Locate and identify every blood parasite.
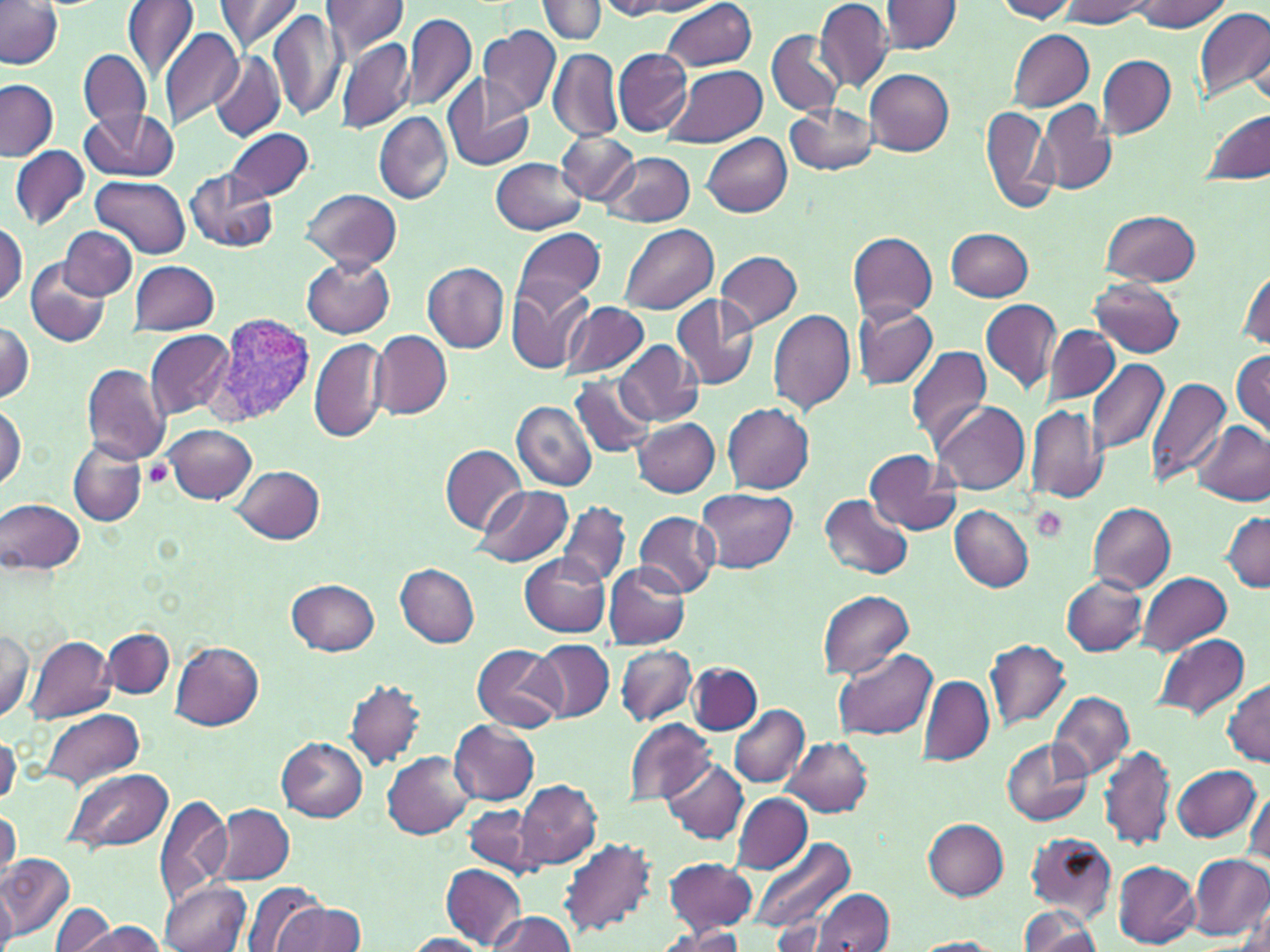
Approximate bounding boxes as (x1, y1, x2, y2) in pixels.
Plasmodium vivax-infected red blood cells: (207, 312, 317, 428).
No Plasmodium falciparum, Plasmodium ovale, Plasmodium malariae, Babesia divergens, or Trypanosoma brucei observed.

Uninfected red blood cell locations: (123, 0, 199, 80), (319, 0, 410, 61), (537, 0, 606, 42), (994, 0, 1077, 21), (1131, 0, 1230, 33), (213, 1, 302, 56), (597, 1, 689, 19), (628, 1, 722, 16), (817, 1, 893, 91), (1061, 1, 1149, 26), (0, 2, 64, 70), (659, 2, 758, 71), (880, 2, 962, 53), (1194, 7, 1270, 104), (269, 10, 345, 123), (402, 12, 477, 114), (478, 24, 561, 118), (158, 28, 243, 130), (767, 28, 843, 116), (1008, 28, 1096, 111), (335, 38, 416, 134), (79, 49, 150, 129), (548, 49, 623, 143), (613, 49, 692, 136), (210, 51, 286, 143), (1097, 56, 1175, 137), (665, 64, 768, 147), (865, 69, 953, 155), (441, 74, 536, 173), (0, 80, 57, 161), (1037, 101, 1116, 196), (785, 102, 879, 177), (980, 105, 1056, 215), (80, 107, 178, 182), (1203, 109, 1269, 185), (374, 112, 453, 204), (224, 126, 315, 203), (556, 129, 639, 205), (702, 133, 792, 217), (10, 146, 88, 230), (602, 153, 695, 229), (490, 158, 585, 233), (185, 170, 277, 253), (91, 176, 189, 259), (301, 189, 403, 271), (1100, 209, 1201, 286), (0, 220, 26, 307), (618, 223, 718, 315), (60, 226, 136, 299), (512, 226, 605, 312), (947, 227, 1033, 300), (849, 232, 938, 323), (717, 250, 803, 332), (304, 257, 395, 339), (26, 260, 110, 347), (129, 260, 218, 334), (423, 262, 509, 353), (1237, 267, 1269, 352), (1090, 279, 1184, 358), (506, 282, 595, 375), (671, 294, 760, 391), (980, 298, 1061, 394), (560, 301, 650, 381), (851, 304, 939, 391), (769, 308, 856, 416), (0, 319, 35, 404), (1044, 324, 1120, 406), (144, 330, 233, 418), (369, 330, 452, 419), (308, 337, 390, 444), (615, 341, 702, 426), (906, 343, 992, 448), (1233, 349, 1270, 436), (1086, 358, 1169, 459), (81, 362, 171, 464), (569, 373, 657, 458), (1146, 375, 1231, 487), (932, 399, 1031, 495), (512, 401, 598, 492), (723, 403, 814, 495), (0, 404, 25, 491), (1025, 404, 1108, 504), (633, 416, 720, 497), (1195, 422, 1270, 506), (164, 424, 257, 504), (68, 438, 147, 527), (439, 443, 527, 533), (863, 449, 960, 535), (233, 464, 325, 544), (473, 484, 573, 567), (696, 486, 797, 573), (820, 494, 913, 579), (2, 500, 85, 574), (557, 500, 630, 589), (543, 502, 647, 645), (1089, 502, 1176, 593), (950, 505, 1033, 592), (1220, 510, 1270, 591), (633, 511, 720, 598), (520, 555, 610, 637), (604, 562, 690, 650), (395, 564, 480, 648), (1136, 572, 1232, 655), (1062, 575, 1148, 657), (287, 579, 379, 656), (817, 590, 914, 679), (0, 628, 36, 724), (102, 628, 176, 699), (1154, 632, 1251, 720), (25, 634, 117, 723), (529, 639, 615, 723), (986, 639, 1071, 729), (171, 641, 263, 731), (470, 643, 565, 734), (615, 644, 695, 725), (833, 648, 935, 739), (688, 663, 763, 734), (917, 675, 994, 765), (344, 678, 427, 770), (1224, 678, 1269, 766), (1048, 690, 1134, 780), (728, 704, 809, 787), (40, 707, 144, 790), (626, 719, 717, 806), (449, 720, 540, 805), (782, 736, 873, 817), (278, 738, 368, 820), (1003, 739, 1091, 827), (1099, 742, 1177, 852), (383, 752, 474, 840), (662, 759, 752, 844), (1172, 763, 1262, 844), (64, 767, 174, 855), (515, 781, 603, 871), (1241, 786, 1269, 869), (732, 792, 812, 873), (154, 793, 231, 907), (215, 804, 294, 884), (466, 805, 543, 877), (2, 809, 20, 873), (0, 819, 16, 898), (923, 819, 1008, 899), (1025, 831, 1118, 920), (751, 837, 856, 936), (558, 838, 656, 939), (1189, 853, 1269, 941), (3, 854, 76, 940), (663, 857, 755, 934), (1113, 861, 1199, 948), (441, 863, 527, 950), (0, 875, 17, 951), (157, 879, 249, 952), (244, 881, 329, 952), (813, 890, 895, 952), (52, 902, 117, 952), (273, 903, 366, 952), (1017, 904, 1101, 952), (1235, 909, 1270, 952), (487, 911, 575, 950), (773, 921, 834, 949), (74, 922, 168, 952), (653, 925, 751, 951), (404, 933, 495, 951), (911, 938, 1004, 952). Platelet locations: (145, 460, 175, 489), (1031, 507, 1068, 544). Slide-level diagnosis: Plasmodium vivax. Image is 1270×952 pixels. One field of a larger specimen. Optical microscopy. May-Grünwald-Giemsa stain. Thin blood smear. 1000x magnification.